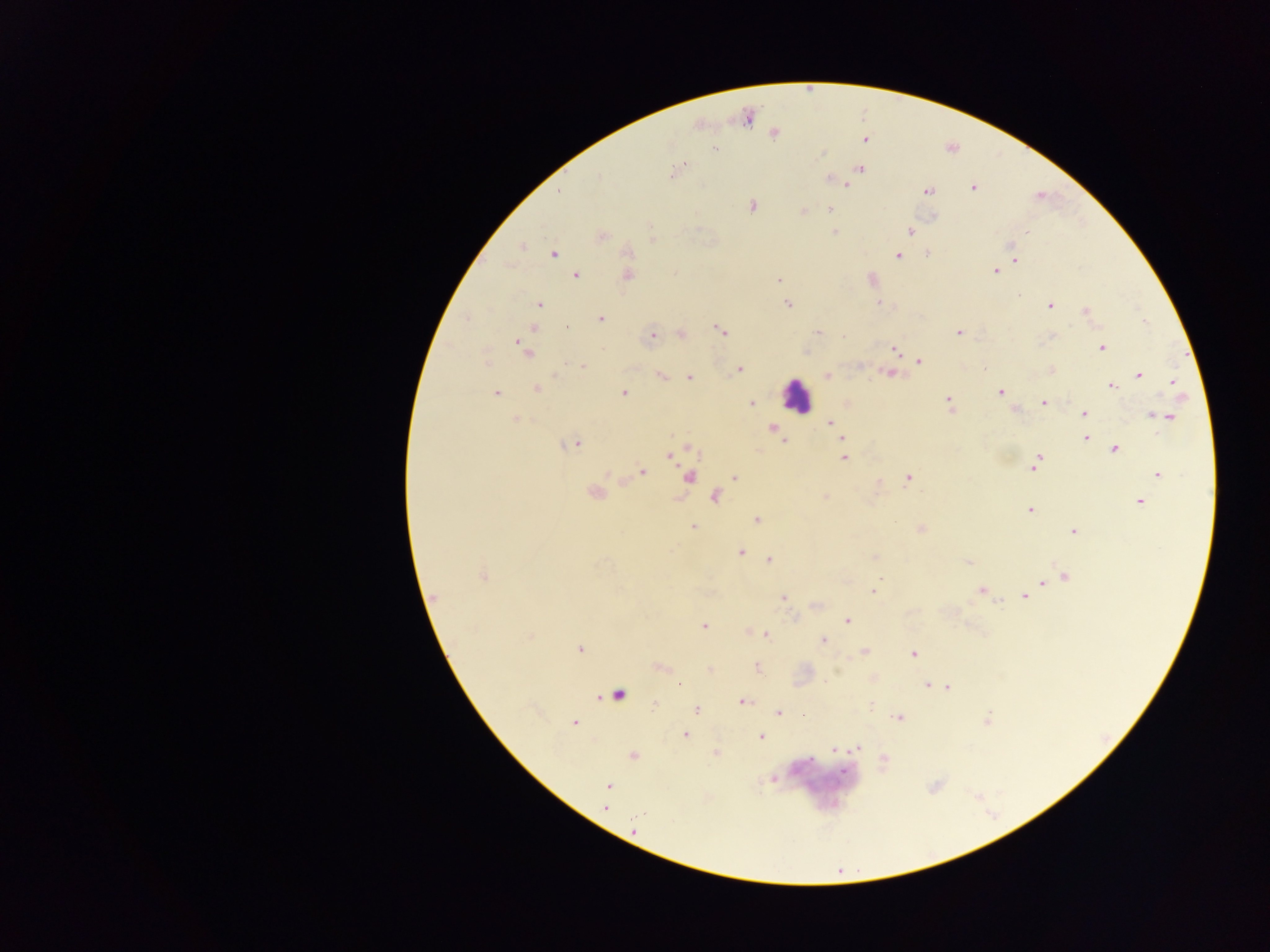
Approximate centers as (x, y) in pixels.
Summary:
  - Leukocyte locations: (797, 395)
  - Malaria parasite locations: (747, 117), (698, 124), (774, 132), (865, 139), (715, 149), (860, 168), (673, 171), (829, 178), (845, 185), (973, 187), (927, 191), (1039, 195), (751, 206), (829, 208), (803, 211), (933, 217), (834, 231), (910, 231), (1026, 232), (600, 235), (652, 240), (521, 245), (627, 252), (553, 253), (927, 253), (898, 255), (1014, 258), (996, 271), (576, 274), (626, 274), (871, 279), (778, 280), (788, 303), (880, 303), (539, 304), (1049, 305), (1085, 311), (600, 319), (533, 327), (722, 331), (817, 332), (958, 332), (681, 335), (651, 337), (1051, 337), (1101, 347), (894, 348), (525, 350), (804, 351), (918, 360), (582, 366), (984, 368), (739, 369), (1052, 370), (890, 373), (661, 375), (826, 375), (1138, 375), (688, 376), (1173, 382), (1112, 386), (537, 388), (623, 392), (1000, 392), (495, 393), (948, 400), (1043, 402), (751, 403), (846, 403), (1014, 408), (1084, 413), (1152, 414), (1157, 415), (1168, 417), (515, 419), (830, 422), (772, 426), (842, 438), (1084, 438), (784, 439), (574, 443), (687, 447), (1114, 448), (670, 454), (844, 457), (1037, 462), (642, 472), (1157, 473), (608, 474), (688, 477), (734, 477), (908, 477), (594, 493), (714, 495), (825, 497), (1139, 502), (1029, 510), (756, 519), (693, 526), (921, 529), (1074, 532), (740, 551), (875, 556), (769, 559), (968, 563), (483, 575), (1064, 575), (1052, 579), (1042, 582), (981, 590), (873, 591), (433, 597), (783, 597), (1024, 597), (815, 604), (846, 620), (703, 625), (749, 631), (758, 632), (766, 635), (822, 640), (579, 648), (863, 651), (913, 653), (659, 666), (757, 667), (709, 669), (873, 678), (678, 684), (927, 685), (948, 687), (617, 694), (741, 701), (655, 704), (695, 708), (778, 712), (898, 718), (986, 719), (574, 722), (685, 734), (761, 737), (857, 747), (835, 749), (716, 752), (632, 755), (883, 760), (773, 779), (608, 786), (605, 807), (634, 830)
  - Capture: mobile-phone photograph through a microscope
  - Image size: 1270×952 pixels
  - Preparation: thick blood smear
  - Field of view: single
  - Country: Ghana